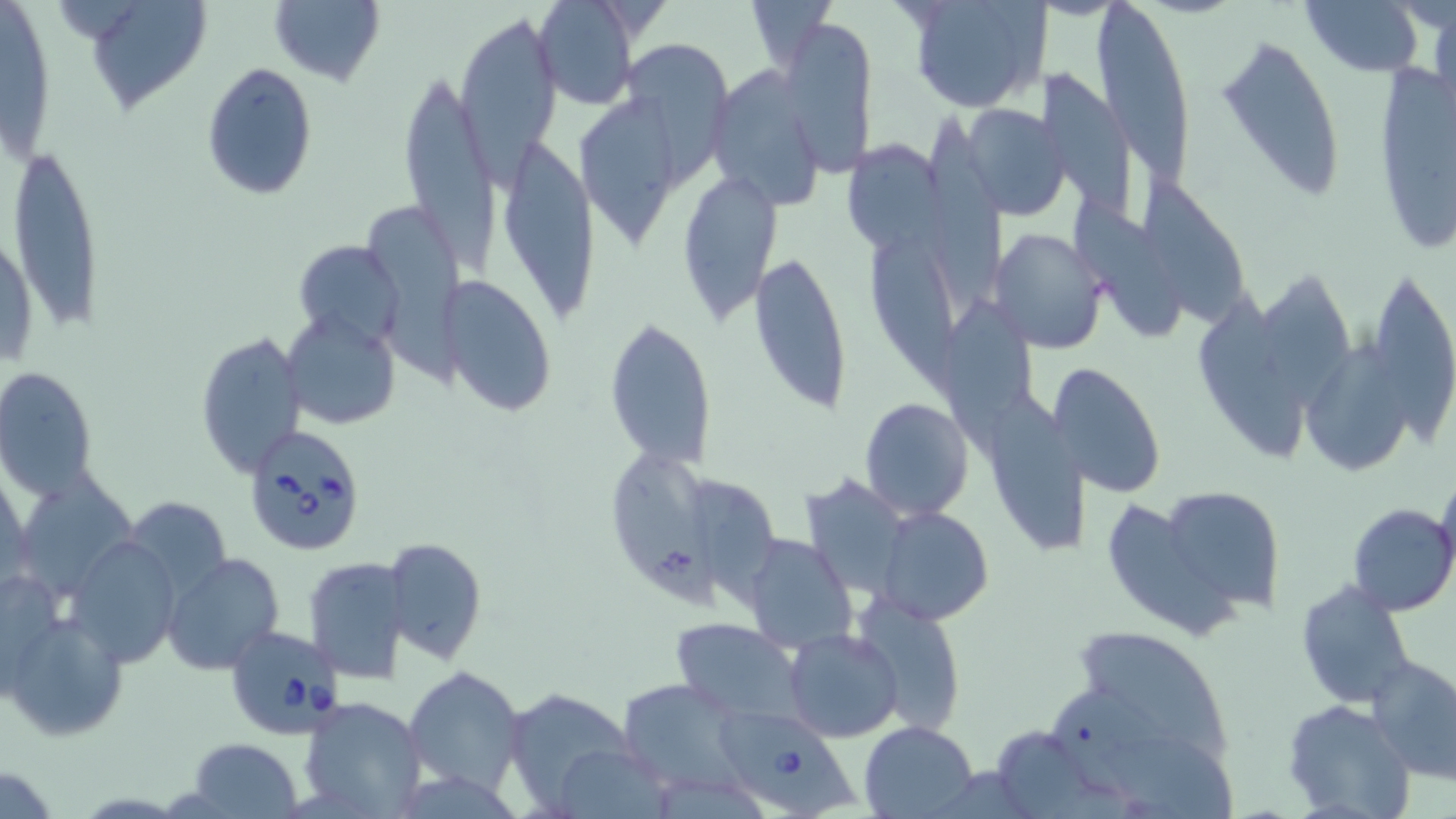

slide-level diagnosis = Babesia divergens
image size = 1456×819 pixels
Babesia divergens-infected red blood cell locations = approximate bounding boxes as [x1, y1, x2, y2] in pixels: [243, 425, 369, 556], [222, 621, 347, 740], [716, 706, 860, 819]
stain = May-Grünwald-Giemsa
magnification = 1000x
preparation = thin blood smear
field of view = single
modality = light microscopy
uninfected red blood cell locations = approximate bounding boxes as [x1, y1, x2, y2] in pixels: [80, 0, 213, 117], [269, 0, 386, 87], [534, 0, 639, 109], [742, 0, 838, 67], [903, 0, 1049, 113], [1300, 0, 1428, 75], [1, 2, 59, 168], [1093, 2, 1193, 178], [450, 12, 561, 167], [779, 17, 877, 174], [1217, 31, 1346, 211], [623, 40, 733, 196], [1373, 62, 1455, 254], [200, 63, 318, 200], [1037, 65, 1138, 214], [400, 66, 497, 270], [707, 66, 828, 210], [581, 95, 677, 250], [958, 102, 1070, 222], [918, 111, 1013, 308], [847, 130, 950, 258], [502, 139, 598, 324], [8, 142, 106, 335], [676, 167, 785, 324], [1141, 175, 1244, 328], [1077, 196, 1186, 345], [369, 208, 478, 391], [1, 225, 37, 373], [861, 227, 959, 395], [991, 229, 1110, 353], [293, 238, 403, 350], [750, 249, 853, 415], [1263, 275, 1353, 411], [1373, 278, 1456, 452], [446, 280, 557, 418], [939, 292, 1039, 452], [1192, 293, 1305, 473], [284, 309, 401, 428], [604, 316, 716, 472], [195, 330, 306, 479], [1306, 338, 1403, 479], [1054, 360, 1165, 500], [0, 366, 99, 499], [995, 395, 1090, 554], [859, 396, 974, 520], [612, 451, 723, 613], [25, 463, 146, 608], [804, 467, 911, 601], [1436, 469, 1456, 589], [687, 474, 785, 616], [1158, 487, 1287, 616], [133, 493, 234, 603], [1103, 499, 1247, 641], [1347, 504, 1456, 616], [876, 506, 993, 621], [1321, 510, 1440, 691], [737, 533, 855, 654], [68, 535, 180, 667], [386, 538, 486, 663], [161, 553, 284, 675], [303, 556, 407, 683], [1296, 581, 1416, 706], [854, 595, 967, 734], [2, 609, 128, 742], [671, 618, 805, 724], [1074, 626, 1229, 765], [784, 628, 903, 743], [1369, 655, 1456, 782], [404, 666, 527, 794], [619, 680, 757, 805], [510, 691, 630, 812], [1048, 691, 1201, 787], [296, 695, 428, 818], [1282, 699, 1415, 819], [859, 719, 981, 818], [989, 725, 1098, 814], [1110, 736, 1234, 819], [186, 737, 303, 817], [557, 750, 666, 819]